Name the parasite shown.
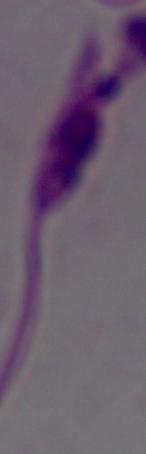

This is Leishmania.

Summary:
  - Modality: micrograph
  - Magnification: 1000x